Assess the morphology of the red blood cells.
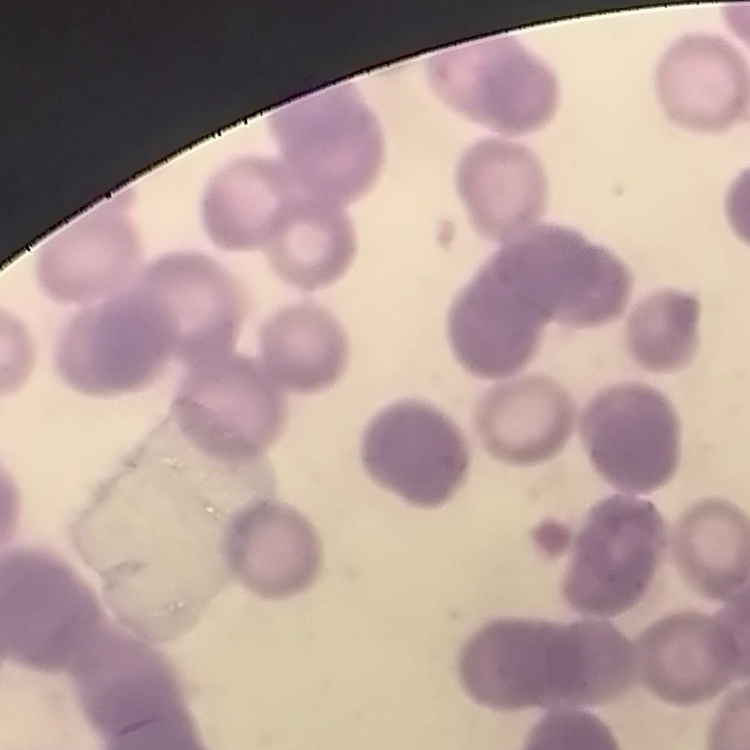

They show rouleaux formation.

image type = square crop of a larger photomicrograph
stain = Field's or Giemsa
preparation = thin blood smear